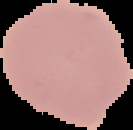

Summary:
  - Image type: segmented cell region on a black background
  - Preparation: thin blood film
  - Result: no Plasmodium parasites detected
  - Image size: 133×130 pixels